Mark where leukocytes are.
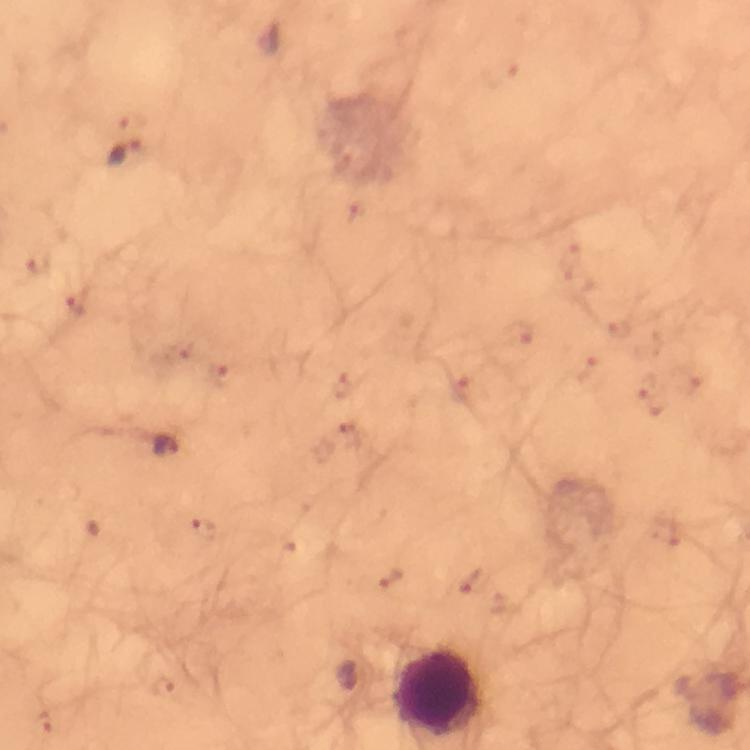

Approximate centers as (x, y) in pixels.
Leukocytes: (439, 691).

Summary:
  - Plasmodium parasite locations: (125, 151), (167, 446)
  - Stain: Giemsa
  - Preparation: thick smear
  - Immersion oil: used
  - Cropped from: a single field of view
  - Capture: smartphone mounted on the microscope
  - Magnification: 100x
  - Context: from a malaria diagnostic workup
  - Image size: 750×750 pixels